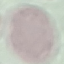

Summary:
  - Result: negative for malaria parasites
  - Capture: smartphone through the microscope eyepiece
  - Image type: cell patch, automatically extracted from a larger field of view and resized to 64 × 64 pixels
  - Preparation: thin blood smear
  - Stain: Giemsa